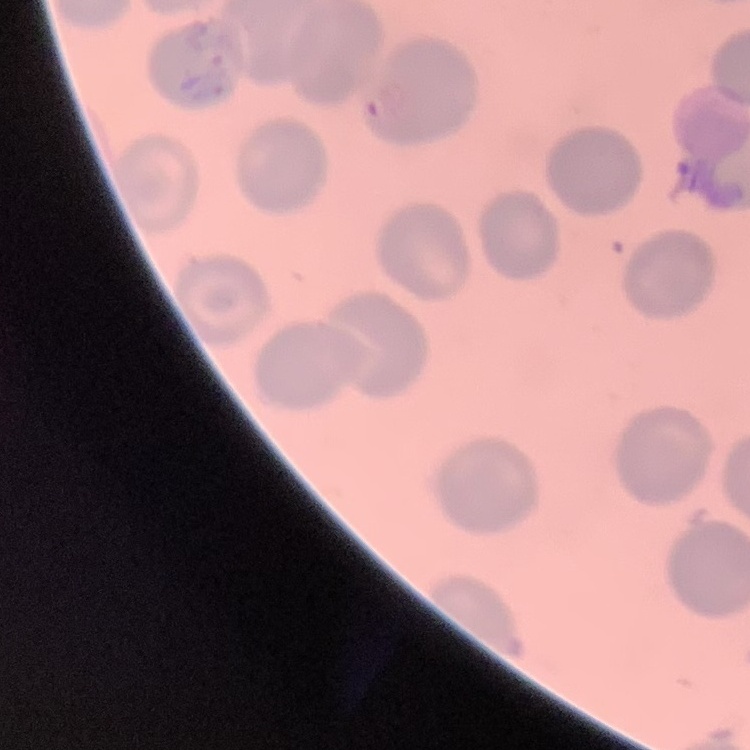

The erythrocytes exhibit no rouleaux formation. Stained with either Field's or Giemsa. Thin blood film. Square crop of a larger photomicrograph.